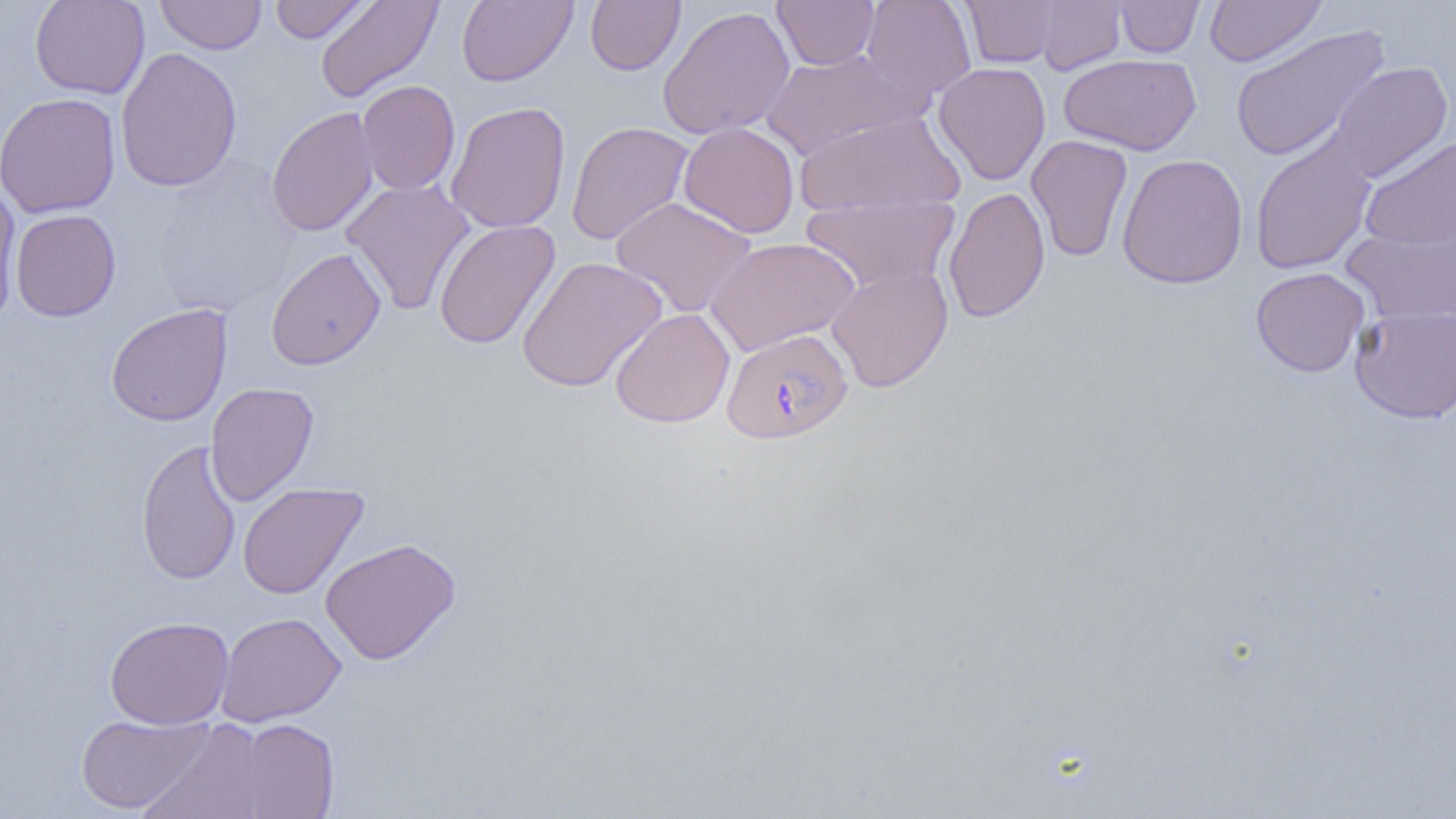

Approximate bounding boxes as named x1/y1/x2/y2 corners in pixels. Uninfected red blood cell locations: (x1=29, y1=0, x2=150, y2=99), (x1=155, y1=0, x2=267, y2=55), (x1=270, y1=0, x2=374, y2=43), (x1=314, y1=0, x2=444, y2=103), (x1=457, y1=0, x2=577, y2=87), (x1=585, y1=0, x2=685, y2=75), (x1=772, y1=0, x2=879, y2=70), (x1=862, y1=0, x2=976, y2=101), (x1=960, y1=0, x2=1060, y2=68), (x1=1034, y1=0, x2=1126, y2=74), (x1=1114, y1=0, x2=1204, y2=57), (x1=1204, y1=0, x2=1327, y2=67), (x1=657, y1=5, x2=795, y2=140), (x1=1230, y1=24, x2=1390, y2=163), (x1=115, y1=47, x2=242, y2=192), (x1=759, y1=49, x2=921, y2=161), (x1=1058, y1=53, x2=1201, y2=155), (x1=933, y1=61, x2=1051, y2=185), (x1=1329, y1=61, x2=1453, y2=183), (x1=357, y1=80, x2=460, y2=196), (x1=0, y1=92, x2=121, y2=218), (x1=445, y1=101, x2=571, y2=233), (x1=266, y1=106, x2=379, y2=237), (x1=794, y1=110, x2=965, y2=217), (x1=566, y1=121, x2=694, y2=246), (x1=679, y1=122, x2=800, y2=238), (x1=1026, y1=134, x2=1133, y2=262), (x1=1249, y1=134, x2=1377, y2=274), (x1=1360, y1=136, x2=1456, y2=250), (x1=1116, y1=153, x2=1248, y2=290), (x1=153, y1=155, x2=302, y2=317), (x1=339, y1=178, x2=476, y2=315), (x1=0, y1=183, x2=22, y2=320), (x1=943, y1=187, x2=1050, y2=323), (x1=800, y1=195, x2=959, y2=293), (x1=610, y1=196, x2=757, y2=318), (x1=10, y1=209, x2=121, y2=322), (x1=433, y1=219, x2=561, y2=350), (x1=1342, y1=222, x2=1456, y2=327), (x1=706, y1=237, x2=860, y2=356), (x1=266, y1=247, x2=386, y2=370), (x1=516, y1=256, x2=667, y2=392), (x1=826, y1=264, x2=954, y2=393), (x1=1250, y1=267, x2=1370, y2=377), (x1=105, y1=303, x2=233, y2=426), (x1=1349, y1=303, x2=1456, y2=423), (x1=609, y1=307, x2=735, y2=428), (x1=205, y1=382, x2=319, y2=507), (x1=135, y1=439, x2=241, y2=586), (x1=238, y1=482, x2=369, y2=600), (x1=320, y1=538, x2=461, y2=665), (x1=216, y1=612, x2=346, y2=726), (x1=104, y1=616, x2=234, y2=729), (x1=75, y1=712, x2=213, y2=814), (x1=234, y1=717, x2=340, y2=818), (x1=137, y1=718, x2=270, y2=819). Plasmodium falciparum-infected red blood cell locations: (x1=721, y1=328, x2=853, y2=444). Slide-level diagnosis: Plasmodium falciparum. One field of a larger specimen. Thin blood film. Image is 1456×819 pixels. Optical microscopy. 1000x magnification.